Draw a bounding box around every artifact (platelet-like body, stain precipitate, or debris).
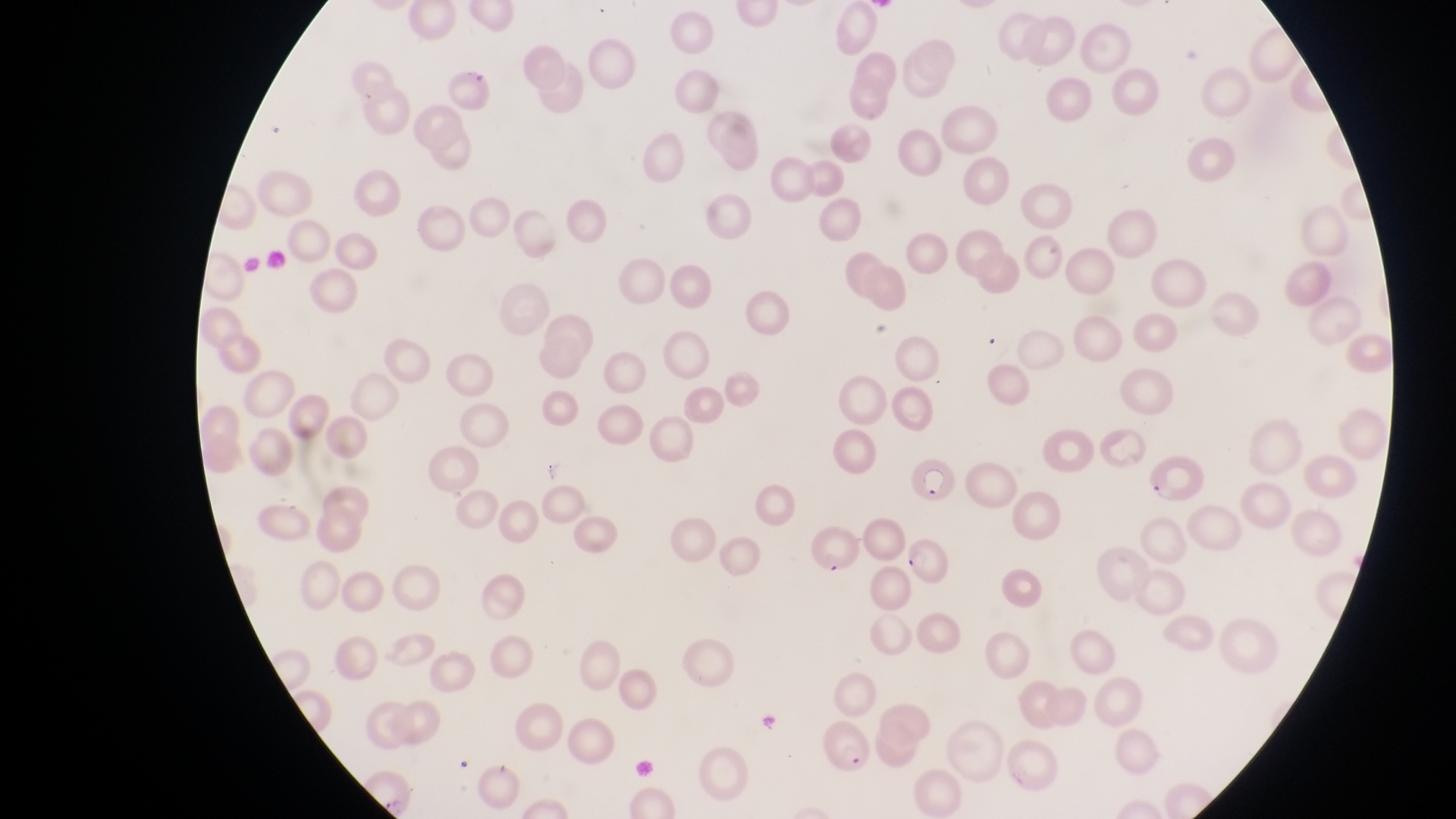
Approximate bounding boxes as left top right bottom in pixels.
Artifacts (platelet-like body, stain precipitate, or debris): 539 460 571 483; 381 792 411 818.

Parasitised red blood cell locations: 1145 453 1205 509; 908 457 957 512; 814 519 855 574; 904 531 953 587; 821 724 877 780. One field of view. At a magnification of 1000x. Sample from Uganda. Captured by a smartphone held over the eyepiece of an Olympus CX-23 microscope. Thin blood smear. Image is 1456×819 pixels.